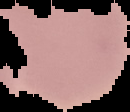 Result: negative for Plasmodium parasites. The area outside the segmented cell region is set to black. From a thin blood smear. Image is 130×112 pixels.